State which parasite is depicted.
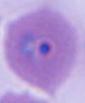
This is Plasmodium.

{
  "modality": "micrograph",
  "magnification": "400x or 1000x"
}